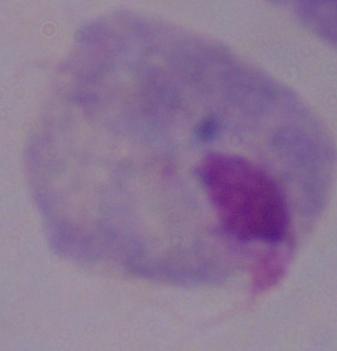
Captured at 1000x magnification. Photomicrograph. A trichomonad is shown.